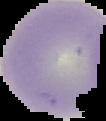
The area outside the segmented cell region is set to black. Malaria status: uninfected. Image is 106×121 pixels. From a thin blood film.